Classify this cell by malaria status.
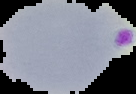

Parasitized.

Summary:
  - Image size: 136×94 pixels
  - Preparation: thin blood film
  - Image type: cell region segmented out of the field of view; surrounding area masked to black